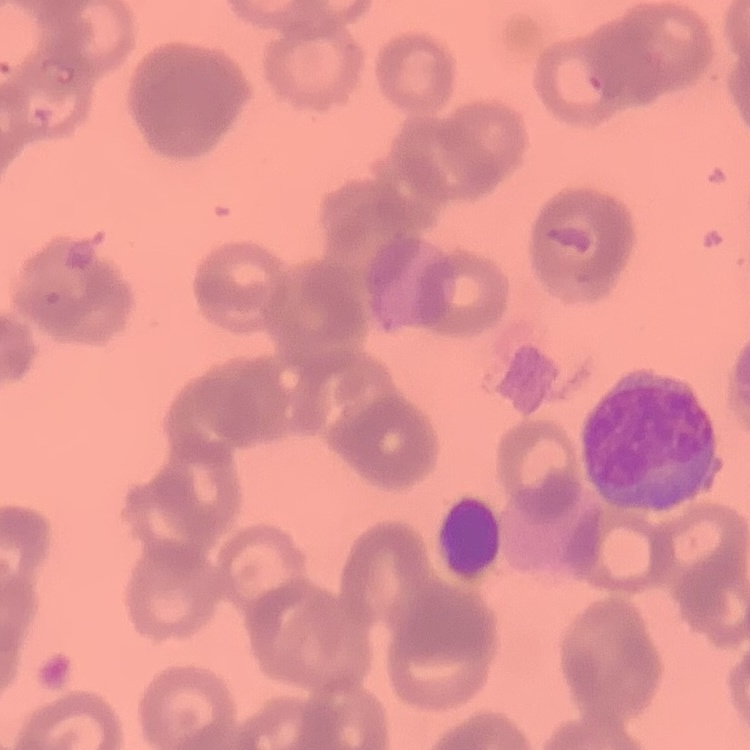

Summary:
  - Red blood cell morphology: rouleaux formation
  - Stain: Field's or Giemsa
  - Image type: one tile cut from a larger photomicrograph
  - Preparation: thin blood film